Name the blood parasite species.
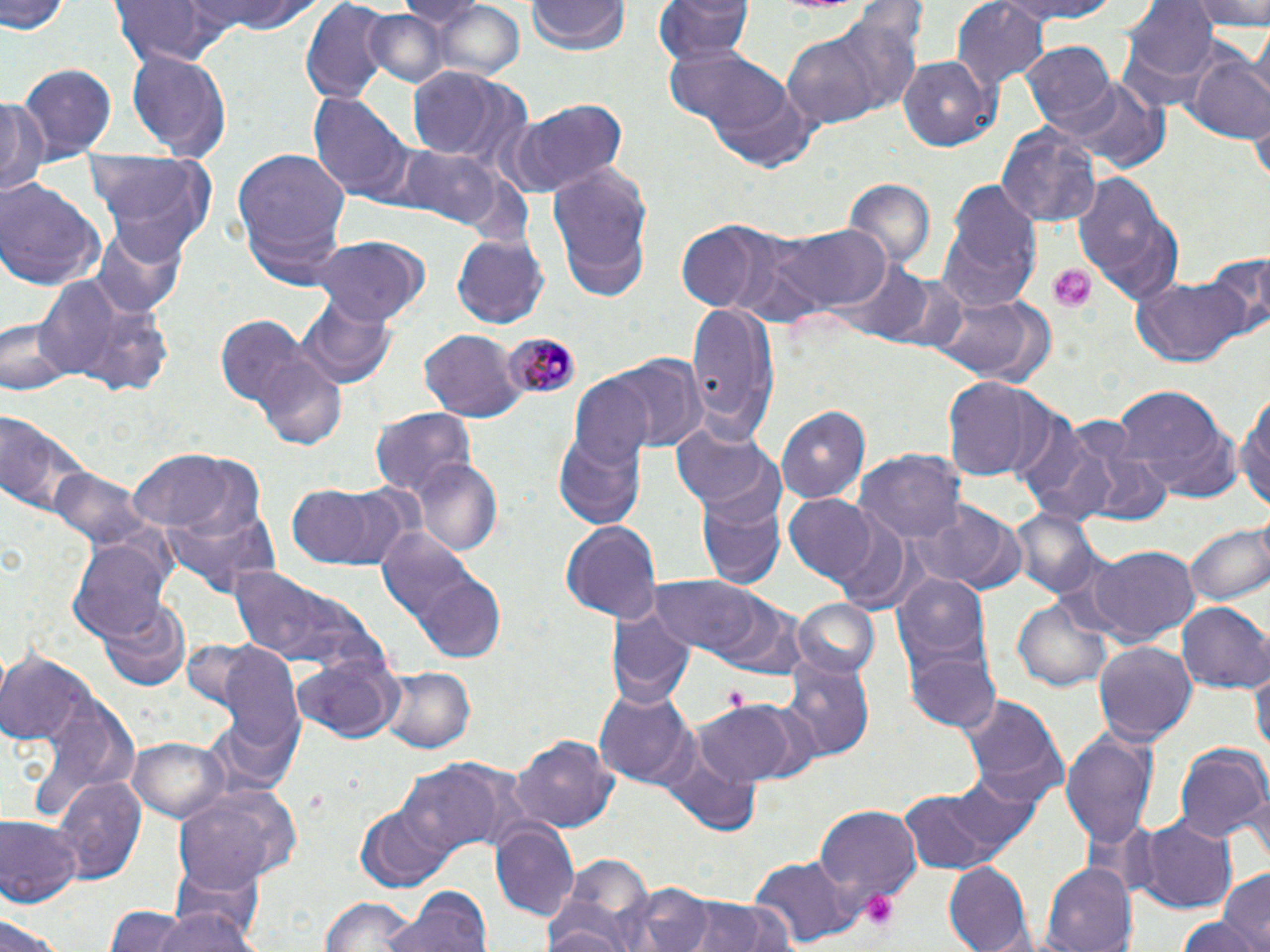
Plasmodium malariae.

Summary:
  - Coordinate format: approximate bounding boxes as named x1/y1/x2/y2 corners in pixels
  - Platelet locations: (x1=1049, y1=264, x2=1094, y2=311), (x1=722, y1=686, x2=750, y2=712), (x1=860, y1=891, x2=899, y2=932)
  - Uninfected red blood cell locations: (x1=2, y1=0, x2=69, y2=37), (x1=189, y1=0, x2=315, y2=37), (x1=400, y1=0, x2=481, y2=38), (x1=656, y1=0, x2=755, y2=71), (x1=988, y1=0, x2=1124, y2=24), (x1=1125, y1=0, x2=1216, y2=84), (x1=1191, y1=0, x2=1270, y2=34), (x1=110, y1=1, x2=237, y2=66), (x1=296, y1=1, x2=392, y2=107), (x1=526, y1=1, x2=628, y2=57), (x1=952, y1=3, x2=1048, y2=90), (x1=428, y1=4, x2=527, y2=81), (x1=362, y1=8, x2=448, y2=87), (x1=781, y1=11, x2=922, y2=130), (x1=1250, y1=24, x2=1270, y2=106), (x1=664, y1=42, x2=803, y2=156), (x1=1023, y1=43, x2=1117, y2=133), (x1=1189, y1=49, x2=1270, y2=143), (x1=127, y1=50, x2=230, y2=162), (x1=897, y1=56, x2=1000, y2=150), (x1=19, y1=62, x2=116, y2=158), (x1=407, y1=67, x2=528, y2=167), (x1=1069, y1=78, x2=1168, y2=172), (x1=310, y1=94, x2=412, y2=200), (x1=0, y1=96, x2=50, y2=201), (x1=503, y1=99, x2=630, y2=197), (x1=1251, y1=114, x2=1270, y2=190), (x1=996, y1=122, x2=1102, y2=227), (x1=398, y1=145, x2=506, y2=227), (x1=229, y1=147, x2=353, y2=279), (x1=87, y1=152, x2=219, y2=263), (x1=547, y1=168, x2=652, y2=285), (x1=1072, y1=171, x2=1182, y2=304), (x1=843, y1=179, x2=936, y2=273), (x1=0, y1=180, x2=104, y2=291), (x1=938, y1=182, x2=1042, y2=313), (x1=771, y1=221, x2=892, y2=315), (x1=89, y1=222, x2=188, y2=318), (x1=674, y1=224, x2=775, y2=310), (x1=718, y1=228, x2=830, y2=328), (x1=452, y1=233, x2=548, y2=328), (x1=310, y1=236, x2=427, y2=326), (x1=1205, y1=253, x2=1270, y2=343), (x1=834, y1=260, x2=932, y2=341), (x1=887, y1=275, x2=968, y2=355), (x1=37, y1=276, x2=127, y2=380), (x1=1130, y1=276, x2=1250, y2=367), (x1=61, y1=291, x2=176, y2=396), (x1=927, y1=294, x2=1053, y2=384), (x1=294, y1=295, x2=394, y2=391), (x1=686, y1=302, x2=780, y2=439), (x1=3, y1=316, x2=69, y2=394), (x1=217, y1=316, x2=308, y2=408), (x1=418, y1=329, x2=522, y2=421), (x1=253, y1=354, x2=348, y2=450), (x1=609, y1=355, x2=705, y2=453), (x1=567, y1=376, x2=658, y2=470), (x1=940, y1=379, x2=1050, y2=484), (x1=1110, y1=383, x2=1238, y2=503), (x1=1236, y1=387, x2=1269, y2=519), (x1=776, y1=405, x2=869, y2=503), (x1=371, y1=408, x2=474, y2=499), (x1=1, y1=415, x2=94, y2=527), (x1=669, y1=422, x2=782, y2=519), (x1=1016, y1=423, x2=1124, y2=525), (x1=553, y1=431, x2=645, y2=529), (x1=1073, y1=439, x2=1175, y2=526), (x1=128, y1=451, x2=252, y2=537), (x1=857, y1=452, x2=964, y2=546), (x1=411, y1=459, x2=502, y2=553), (x1=50, y1=469, x2=154, y2=555), (x1=285, y1=480, x2=412, y2=573), (x1=695, y1=492, x2=784, y2=588), (x1=783, y1=495, x2=881, y2=585), (x1=158, y1=496, x2=282, y2=603), (x1=913, y1=504, x2=1027, y2=595), (x1=1008, y1=507, x2=1104, y2=601), (x1=560, y1=518, x2=661, y2=622), (x1=1185, y1=518, x2=1270, y2=609), (x1=376, y1=523, x2=477, y2=631), (x1=69, y1=539, x2=172, y2=642), (x1=1080, y1=545, x2=1201, y2=644), (x1=225, y1=563, x2=372, y2=675), (x1=892, y1=571, x2=994, y2=678), (x1=421, y1=576, x2=508, y2=658), (x1=650, y1=576, x2=766, y2=656), (x1=708, y1=592, x2=806, y2=677), (x1=1013, y1=598, x2=1113, y2=692), (x1=101, y1=599, x2=189, y2=691), (x1=602, y1=599, x2=692, y2=711), (x1=791, y1=600, x2=880, y2=680), (x1=1178, y1=602, x2=1269, y2=692), (x1=1092, y1=641, x2=1196, y2=745), (x1=217, y1=649, x2=306, y2=761), (x1=904, y1=649, x2=1001, y2=734), (x1=0, y1=652, x2=91, y2=748), (x1=292, y1=652, x2=401, y2=744), (x1=780, y1=654, x2=876, y2=760), (x1=1251, y1=662, x2=1269, y2=766), (x1=377, y1=667, x2=475, y2=754), (x1=596, y1=690, x2=695, y2=787), (x1=955, y1=694, x2=1067, y2=810), (x1=695, y1=704, x2=804, y2=786), (x1=202, y1=713, x2=300, y2=803), (x1=1061, y1=728, x2=1157, y2=857), (x1=508, y1=733, x2=619, y2=834), (x1=128, y1=739, x2=229, y2=823), (x1=1172, y1=739, x2=1268, y2=844), (x1=398, y1=761, x2=524, y2=855), (x1=54, y1=776, x2=148, y2=882), (x1=175, y1=783, x2=302, y2=885), (x1=896, y1=786, x2=1018, y2=876), (x1=355, y1=804, x2=459, y2=892), (x1=815, y1=804, x2=922, y2=907), (x1=1, y1=816, x2=81, y2=906), (x1=1136, y1=819, x2=1236, y2=913), (x1=489, y1=820, x2=578, y2=921), (x1=560, y1=853, x2=654, y2=942), (x1=748, y1=855, x2=853, y2=948), (x1=166, y1=859, x2=266, y2=944), (x1=942, y1=861, x2=1033, y2=952), (x1=1039, y1=862, x2=1136, y2=952), (x1=1217, y1=869, x2=1270, y2=949), (x1=630, y1=882, x2=716, y2=952), (x1=385, y1=887, x2=491, y2=952), (x1=317, y1=894, x2=422, y2=951), (x1=682, y1=897, x2=796, y2=952), (x1=541, y1=904, x2=641, y2=951), (x1=151, y1=905, x2=259, y2=952), (x1=101, y1=909, x2=192, y2=952), (x1=0, y1=910, x2=68, y2=951), (x1=1173, y1=913, x2=1262, y2=951)
  - Plasmodium malariae-infected red blood cell locations: (x1=501, y1=331, x2=579, y2=402)
  - Field of view: single
  - Magnification: 1000x
  - Image size: 1270×952 pixels
  - Modality: light microscopy
  - Preparation: thin blood smear
  - Stain: May-Grünwald-Giemsa